Locate platelets.
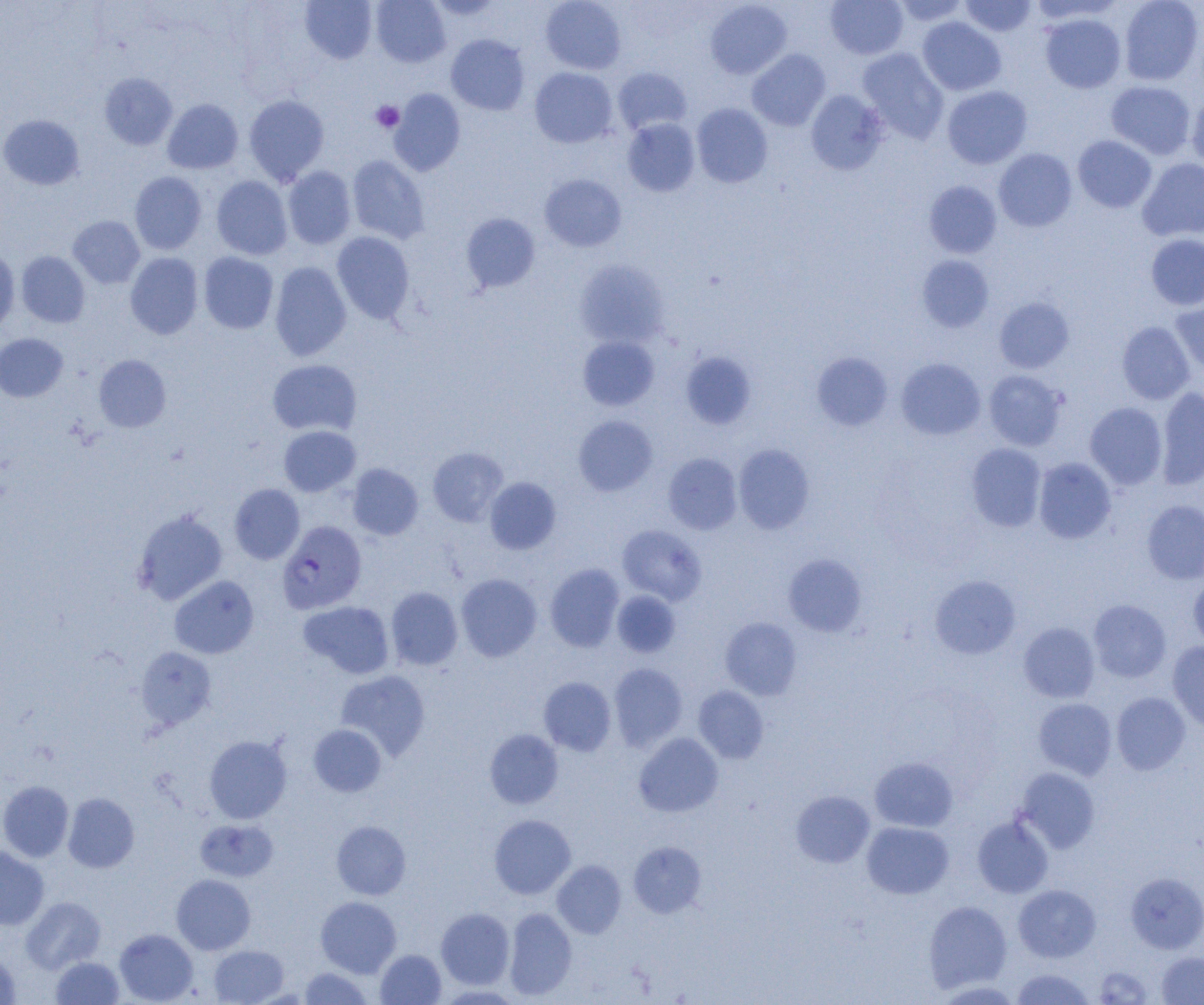
Approximate bounding boxes as (x1, y1, x2, y2) in pixels.
Platelets: (370, 101, 404, 133).

Uninfected red blood cell locations: (370, 0, 450, 67), (426, 0, 505, 19), (540, 0, 626, 74), (705, 0, 792, 79), (825, 0, 908, 59), (891, 0, 971, 27), (959, 0, 1037, 36), (1028, 0, 1125, 25), (1119, 0, 1203, 86), (300, 1, 378, 64), (1040, 13, 1127, 93), (917, 17, 1006, 95), (446, 34, 530, 115), (857, 48, 949, 143), (747, 49, 831, 131), (613, 66, 692, 135), (529, 67, 618, 148), (99, 73, 178, 150), (1105, 81, 1196, 159), (942, 85, 1032, 169), (389, 89, 466, 176), (805, 90, 889, 175), (244, 95, 329, 185), (1186, 95, 1204, 173), (162, 99, 243, 174), (692, 103, 773, 188), (0, 115, 84, 190), (622, 118, 700, 196), (1073, 135, 1157, 213), (994, 148, 1077, 231), (347, 155, 429, 245), (1137, 157, 1204, 242), (283, 166, 356, 249), (129, 171, 207, 254), (539, 173, 627, 252), (211, 175, 293, 260), (924, 180, 1002, 259), (461, 213, 540, 293), (68, 216, 145, 288), (332, 231, 414, 324), (1146, 233, 1204, 310), (0, 245, 20, 333), (16, 251, 90, 328), (125, 252, 203, 339), (198, 252, 278, 334), (917, 255, 994, 332), (575, 259, 670, 349), (270, 261, 351, 361), (1170, 295, 1204, 378), (994, 297, 1074, 373), (1117, 321, 1195, 404), (0, 333, 68, 402), (577, 335, 659, 411), (680, 351, 756, 430), (812, 352, 893, 431), (94, 354, 171, 432), (896, 358, 986, 440), (268, 359, 362, 436), (983, 370, 1067, 451), (1156, 387, 1204, 489), (1085, 402, 1167, 489), (573, 415, 657, 496), (279, 425, 360, 496), (733, 443, 815, 534), (966, 443, 1046, 532), (428, 448, 508, 527), (663, 453, 742, 535), (1034, 457, 1116, 544), (348, 463, 423, 540), (485, 477, 560, 554), (229, 484, 305, 564), (1142, 500, 1204, 584), (132, 509, 228, 605), (617, 524, 707, 606), (783, 554, 867, 637), (545, 563, 624, 652), (455, 573, 542, 662), (1188, 573, 1204, 652), (930, 574, 1021, 659), (169, 576, 259, 659), (386, 586, 463, 670), (612, 591, 681, 658), (1088, 599, 1171, 682), (299, 600, 395, 679), (720, 617, 802, 700), (1019, 622, 1100, 703), (1167, 642, 1204, 731), (135, 647, 216, 729), (609, 663, 687, 751), (335, 670, 430, 761), (538, 676, 616, 756), (693, 686, 769, 763), (1111, 692, 1191, 775), (1033, 697, 1117, 780), (309, 724, 386, 797), (485, 729, 563, 809), (634, 733, 723, 817), (204, 735, 292, 823), (869, 756, 958, 831), (1014, 767, 1100, 853), (0, 780, 73, 862), (790, 790, 875, 868), (63, 792, 139, 872), (489, 814, 576, 899), (972, 816, 1053, 898), (196, 819, 278, 882), (331, 820, 411, 900), (861, 821, 954, 899), (628, 842, 706, 917), (0, 846, 49, 930), (552, 860, 626, 938), (1125, 872, 1204, 953), (171, 874, 256, 954), (1013, 884, 1101, 962), (315, 896, 401, 977), (21, 897, 106, 973), (923, 900, 1012, 992), (504, 907, 577, 1000), (436, 908, 515, 989), (114, 928, 198, 1004), (115, 940, 288, 1003), (209, 944, 288, 1004), (0, 949, 21, 1004), (375, 949, 446, 1004), (1156, 951, 1204, 1004), (50, 956, 125, 1004), (1093, 965, 1154, 1004), (298, 967, 372, 1004), (1010, 969, 1095, 1004). Plasmodium falciparum-infected red blood cell locations: (277, 520, 367, 614). Slide-level diagnosis: Plasmodium falciparum. Thin blood smear. Single field of view. 1000x magnification. Image is 1204×1005 pixels. Optical microscopy.